Describe the morphology of the red blood cells.
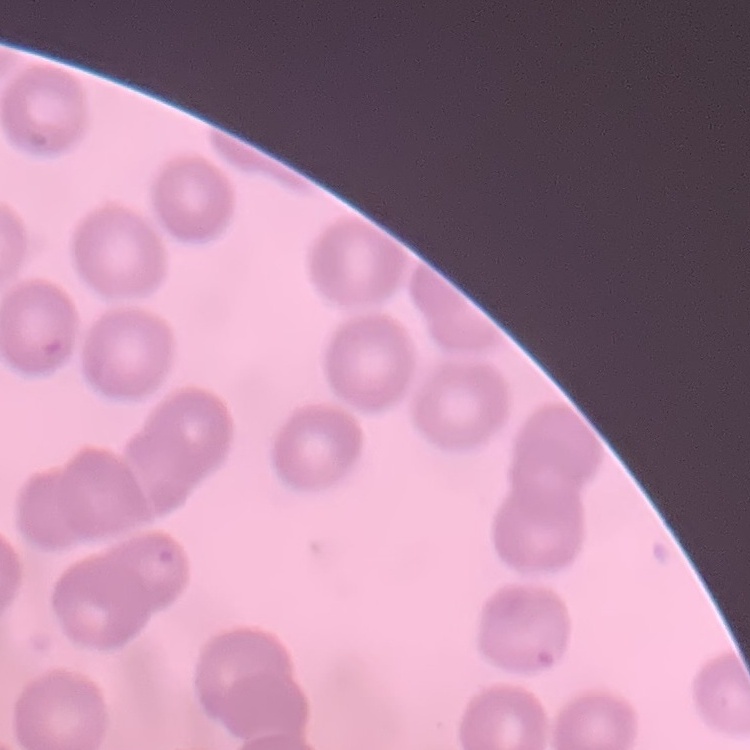

They show no rouleaux formation.

Summary:
  - Stain: Field's or Giemsa
  - Preparation: thin peripheral smear
  - Image type: square crop of a larger photomicrograph